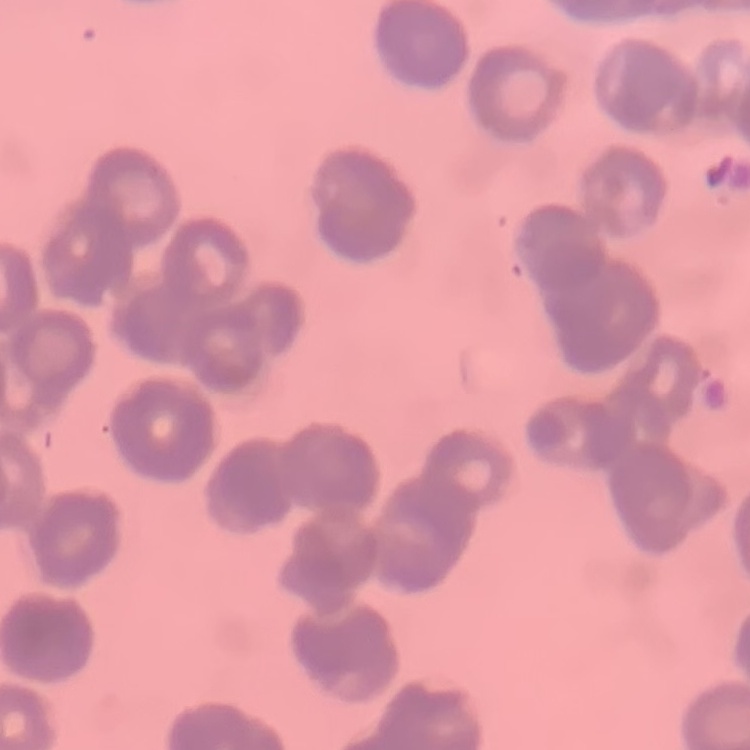

The red blood cells exhibit rouleaux formation. Stained with either Field's or Giemsa. Thin peripheral smear. Square crop of a larger photomicrograph.